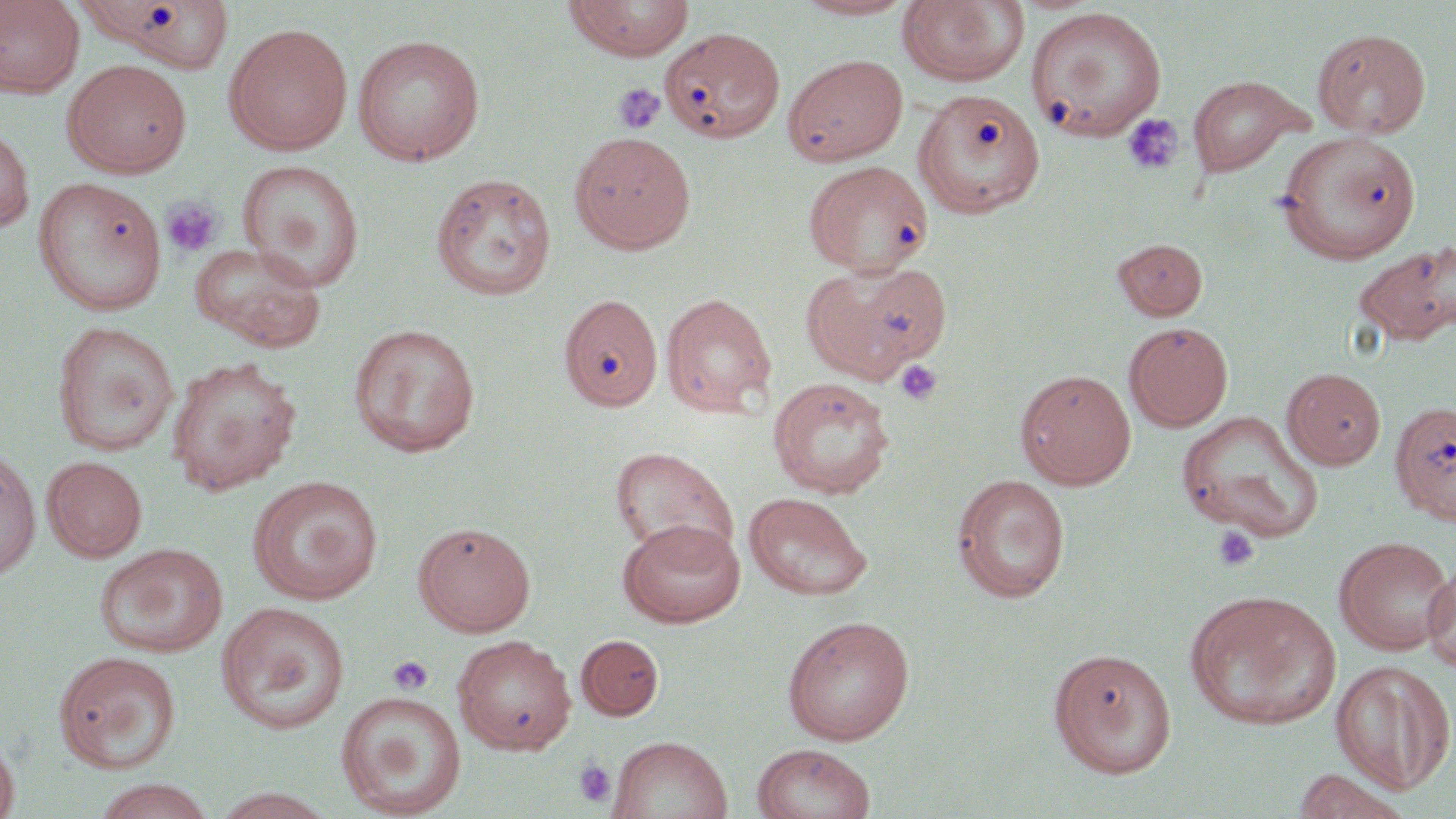

slide-level diagnosis = negative for blood parasites
uninfected red blood cell locations = approximate bounding boxes as (x1, y1, x2, y2) in pixels: (0, 0, 84, 97), (77, 0, 237, 73), (563, 0, 696, 61), (793, 0, 918, 20), (897, 0, 1030, 88), (1027, 7, 1166, 139), (224, 22, 353, 156), (662, 26, 784, 143), (1312, 27, 1431, 139), (351, 34, 485, 165), (782, 53, 909, 166), (62, 59, 192, 178), (1187, 74, 1313, 178), (913, 88, 1046, 218), (0, 123, 35, 233), (569, 131, 697, 254), (1277, 131, 1422, 264), (237, 159, 365, 292), (803, 160, 934, 276), (431, 172, 557, 301), (33, 177, 167, 316), (1113, 238, 1208, 320), (1351, 240, 1455, 347), (189, 243, 327, 352), (803, 260, 952, 382), (660, 292, 777, 416), (558, 294, 663, 412), (51, 321, 180, 456), (1124, 322, 1233, 432), (347, 323, 482, 456), (165, 356, 303, 495), (1282, 367, 1387, 469), (1015, 368, 1137, 489), (768, 375, 895, 498), (1389, 400, 1456, 525), (1178, 411, 1324, 542), (610, 445, 738, 562), (0, 449, 41, 582), (41, 455, 147, 562), (952, 474, 1071, 602), (247, 476, 384, 605), (744, 491, 873, 601), (617, 518, 746, 628), (412, 520, 536, 637), (1334, 536, 1455, 655), (94, 543, 229, 657), (1422, 559, 1456, 674), (1184, 588, 1342, 731), (216, 601, 350, 733), (782, 615, 915, 745), (576, 634, 664, 721), (452, 635, 577, 754), (1048, 647, 1177, 777), (53, 650, 182, 774), (1331, 660, 1455, 793), (335, 692, 467, 817), (0, 732, 20, 819), (607, 735, 732, 819), (752, 743, 876, 819), (91, 778, 217, 819), (209, 786, 341, 819)
field of view = single
preparation = thin blood smear
platelet locations = approximate bounding boxes as (x1, y1, x2, y2) in pixels: (613, 82, 666, 136), (1121, 114, 1185, 176), (160, 196, 223, 258), (894, 359, 944, 406), (1212, 526, 1260, 572), (387, 655, 434, 696), (572, 758, 617, 808)
modality = optical microscopy
magnification = 1000x
image size = 1456×819 pixels
stain = May-Grünwald-Giemsa